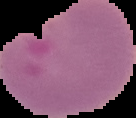
{
  "preparation": "thin blood smear",
  "image_type": "segmented cell region with the area outside set to black",
  "malaria_status": "parasitized",
  "image_size": "136×118 pixels"
}